Locate every Plasmodium vivax-infected red blood cell.
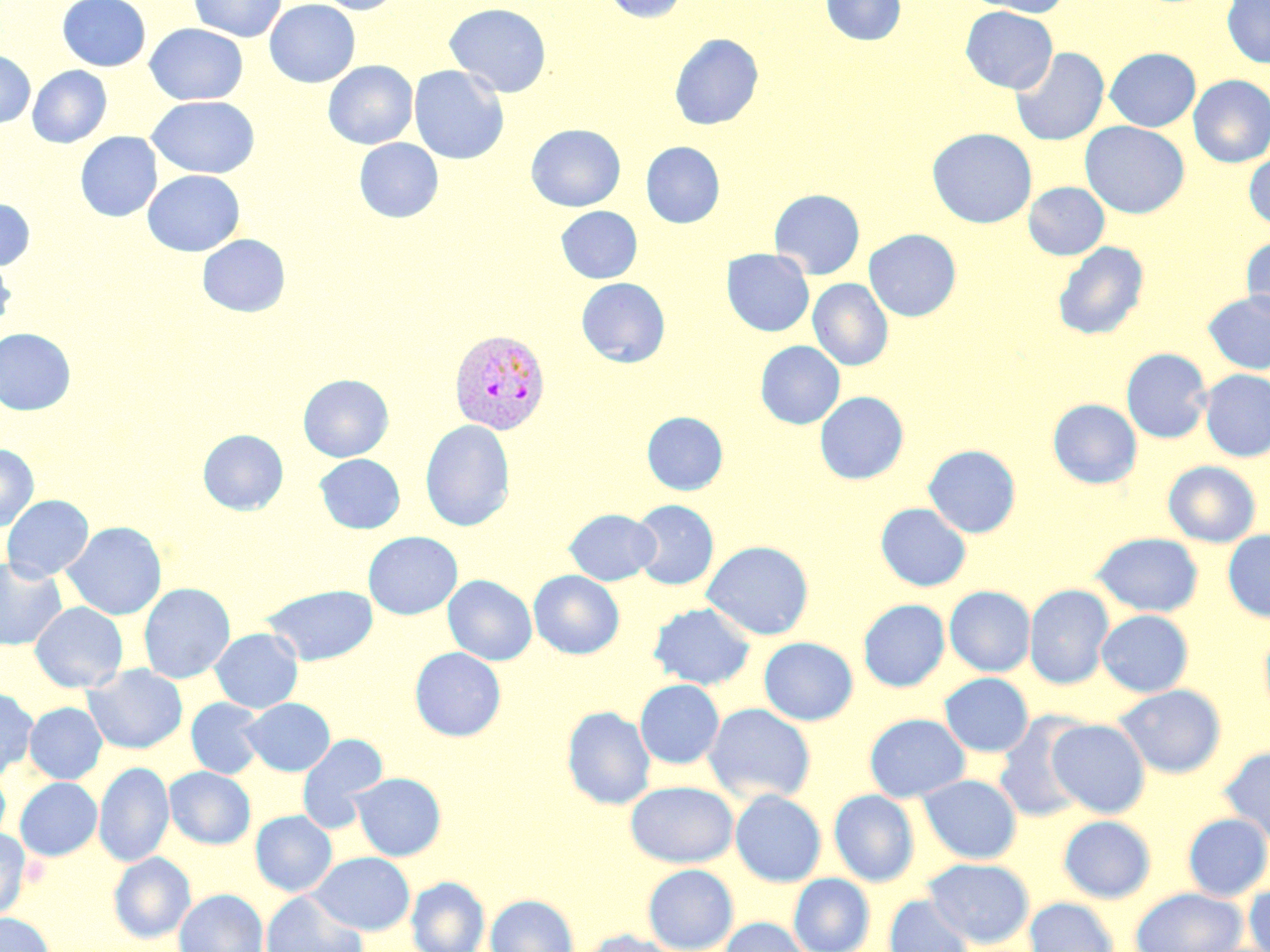
Approximate bounding boxes as (x1,y1)-(x2,y2) corner pairs in pixels.
Plasmodium vivax-infected red blood cells: (449,328)-(551,434).

Summary:
  - Uninfected red blood cell locations: (57,0)-(151,72), (189,0)-(286,42), (265,0)-(360,88), (310,0)-(403,14), (601,0)-(689,23), (821,0)-(906,45), (966,0)-(1070,17), (1222,0)-(1270,68), (444,3)-(552,98), (960,6)-(1058,93), (145,23)-(248,105), (670,33)-(763,130), (1010,47)-(1109,146), (1105,47)-(1200,131), (0,50)-(35,128), (323,60)-(418,149), (27,65)-(111,148), (408,65)-(509,164), (1188,75)-(1270,167), (146,95)-(260,178), (1080,121)-(1189,219), (525,124)-(625,211), (927,127)-(1037,228), (75,132)-(162,222), (354,138)-(443,222), (641,141)-(725,228), (1244,152)-(1270,230), (142,170)-(245,256), (1024,182)-(1109,259), (769,189)-(865,279), (0,198)-(35,270), (556,206)-(642,283), (864,229)-(961,321), (197,234)-(290,317), (1241,235)-(1270,319), (1052,241)-(1149,340), (721,248)-(814,337), (0,255)-(16,333), (576,277)-(670,367), (808,279)-(893,371), (1203,290)-(1270,374), (0,328)-(75,414), (755,340)-(845,429), (1121,348)-(1212,444), (1199,369)-(1270,461), (298,374)-(393,462), (814,391)-(909,485), (1047,398)-(1142,489), (642,411)-(728,495), (420,419)-(515,532), (198,429)-(288,515), (0,443)-(39,532), (924,444)-(1021,538), (314,454)-(404,533), (1163,460)-(1260,547), (2,494)-(93,581), (629,499)-(719,590), (875,503)-(971,591), (565,508)-(660,585), (62,521)-(166,620), (1223,529)-(1270,622), (363,531)-(462,620), (1091,532)-(1204,617), (702,540)-(815,640), (0,556)-(67,651), (528,570)-(624,659), (443,575)-(537,665), (139,583)-(235,683), (262,584)-(379,665), (1025,584)-(1114,689), (944,586)-(1036,676), (858,599)-(950,691), (29,601)-(127,693), (648,603)-(757,690), (1097,610)-(1193,697), (1259,626)-(1270,725), (211,628)-(303,713), (759,637)-(858,725), (410,647)-(506,741), (84,664)-(187,754), (939,673)-(1034,757), (634,679)-(724,769), (1114,684)-(1227,779), (0,686)-(38,780), (241,697)-(335,776), (186,698)-(265,779), (24,702)-(107,784), (704,703)-(816,804), (562,706)-(655,810), (864,713)-(970,803), (994,713)-(1091,822), (1047,718)-(1151,817), (296,733)-(388,833), (1218,747)-(1270,843), (94,761)-(175,867), (0,766)-(11,846), (164,766)-(256,849), (348,772)-(446,861), (918,774)-(1022,864), (15,777)-(102,861), (625,780)-(739,868), (730,789)-(827,887), (828,789)-(920,887), (251,810)-(337,896), (1182,813)-(1270,901), (1058,815)-(1156,903), (0,828)-(32,919), (108,852)-(195,943), (309,852)-(415,935), (923,857)-(1035,948), (643,864)-(738,951), (788,873)-(875,952), (406,877)-(489,952), (1244,881)-(1270,952), (1130,887)-(1247,952), (174,889)-(268,952), (261,890)-(368,952), (486,894)-(578,952), (883,894)-(976,952), (1024,897)-(1119,952), (0,913)-(54,952), (720,917)-(812,952), (576,929)-(683,952)
  - Slide-level diagnosis: Plasmodium vivax
  - Stain: May-Grünwald-Giemsa
  - Image size: 1270×952 pixels
  - Magnification: 1000x
  - Field of view: one of a larger specimen
  - Modality: light microscopy
  - Preparation: thin blood smear